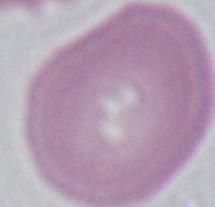

Captured at 1000x magnification. Photomicrograph. A red blood cell is shown.